Locate every Plasmodium parasite.
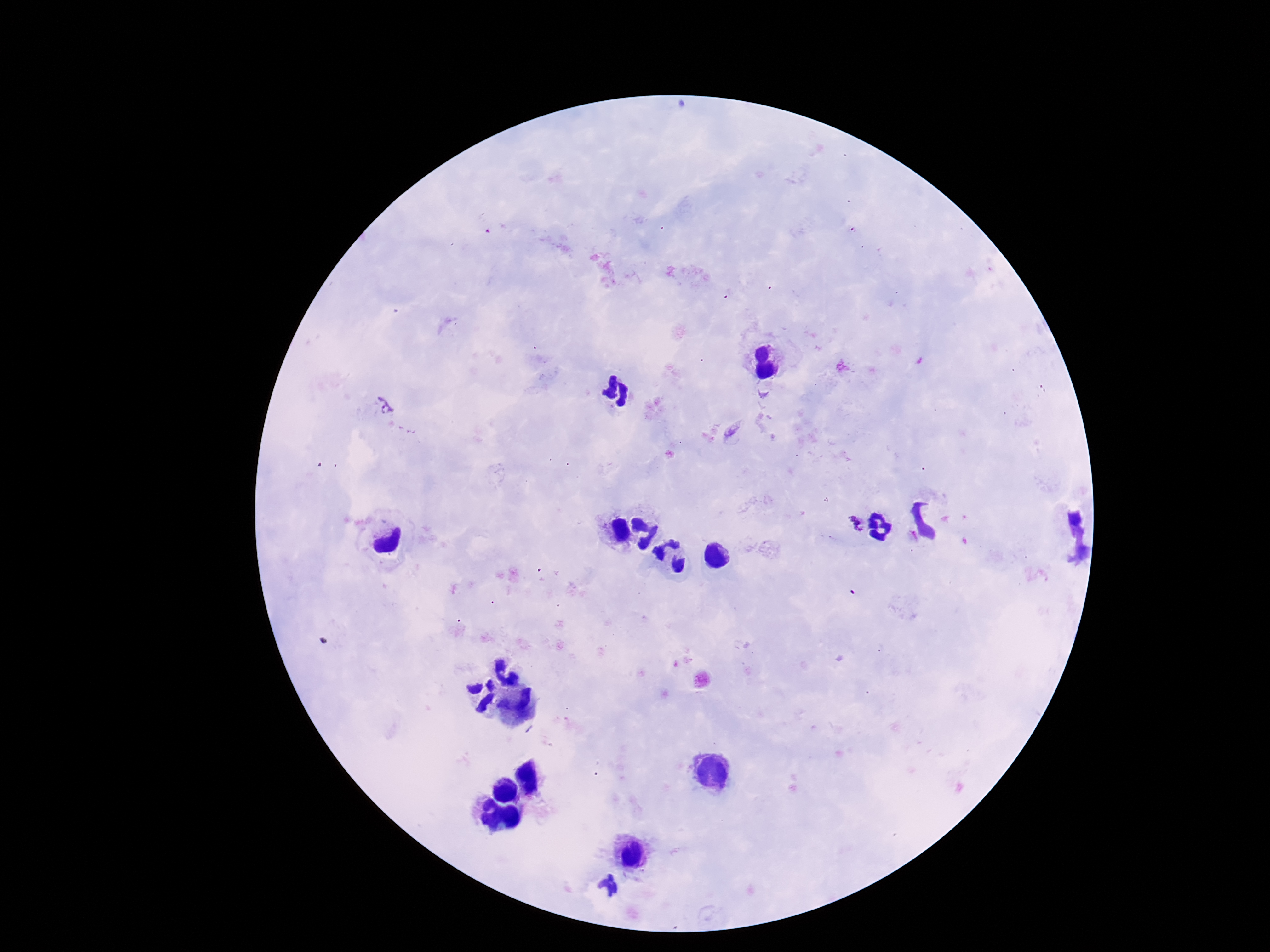
Approximate centers as [x, y] in pixels.
Plasmodium parasites: [386, 409], [855, 524].

Patient malaria status: infected. 100x magnification. Thick blood film. Single field of view. Photographed through the microscope eyepiece with a smartphone camera. Giemsa stain. Image is 1270×952 pixels.